Assess this cell for malaria.
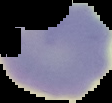
It is uninfected.

From a thin blood smear. Segmented cell region on a black background. Image is 112×103 pixels.